Assess this cell for malaria.
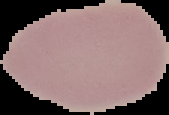
Uninfected.

image type = segmented cell region on a black background
preparation = thin blood film
image size = 169×115 pixels